Give the preparation type.
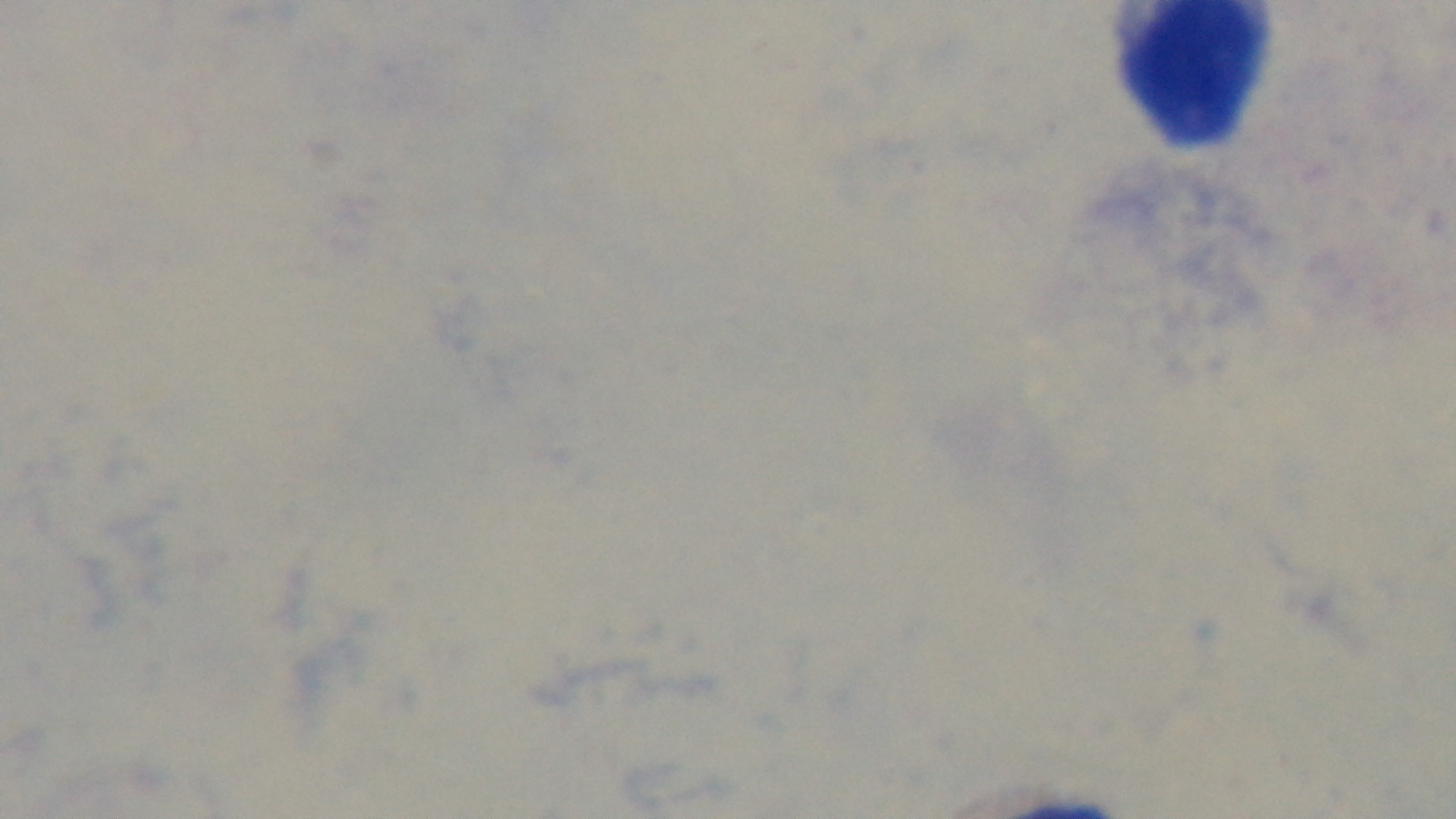

It is a thick blood film.

Summary:
  - Stain: Giemsa
  - Objective: 100x oil immersion
  - Modality: light microscopy
  - Field of view: single
  - Malaria status: negative
  - Capture: mounted 4K digital camera